Assess this cell for malaria.
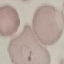
Parasitized.

Thin blood smear. Cell patch, automatically extracted from a larger field of view and resized to 64 × 64 pixels. Acquired by smartphone through the microscope eyepiece. Giemsa-stained preparation.